Assess this cell for malaria.
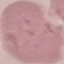

It is uninfected.

Automatically extracted cell patch, resized to 64 × 64 pixels. Giemsa-stained preparation. Thin smear of blood. Acquired by smartphone through the microscope eyepiece.